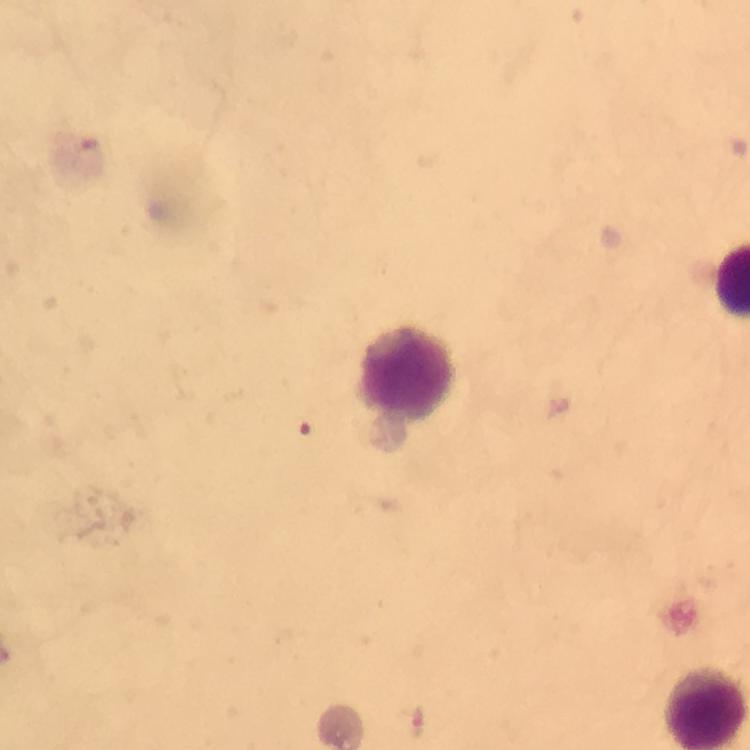

{
  "image_size": "750×750 pixels",
  "malaria_parasite_locations": "approximate object centers, in pixels from the top-left corner: (x=417, y=722)",
  "immersion_oil": "applied",
  "context": "from a diagnostic examination for malaria",
  "cropped_from": "a single field of view",
  "stain": "Giemsa",
  "capture": "smartphone mounted on the microscope",
  "preparation": "thick blood smear",
  "magnification": "100x"
}